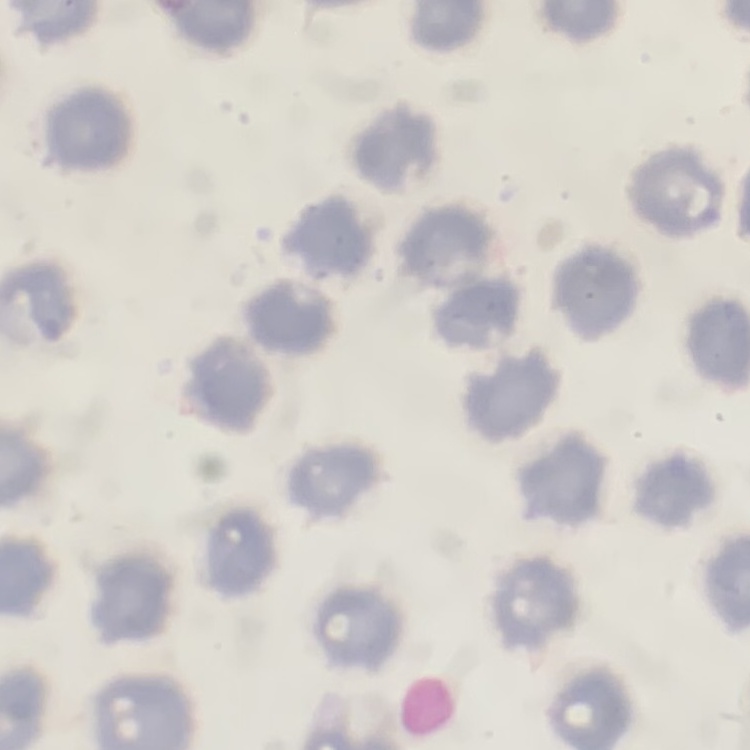

The red blood cells show no rouleaux formation. Square crop of a larger photomicrograph. Thin blood film. Field's or Giemsa stain.